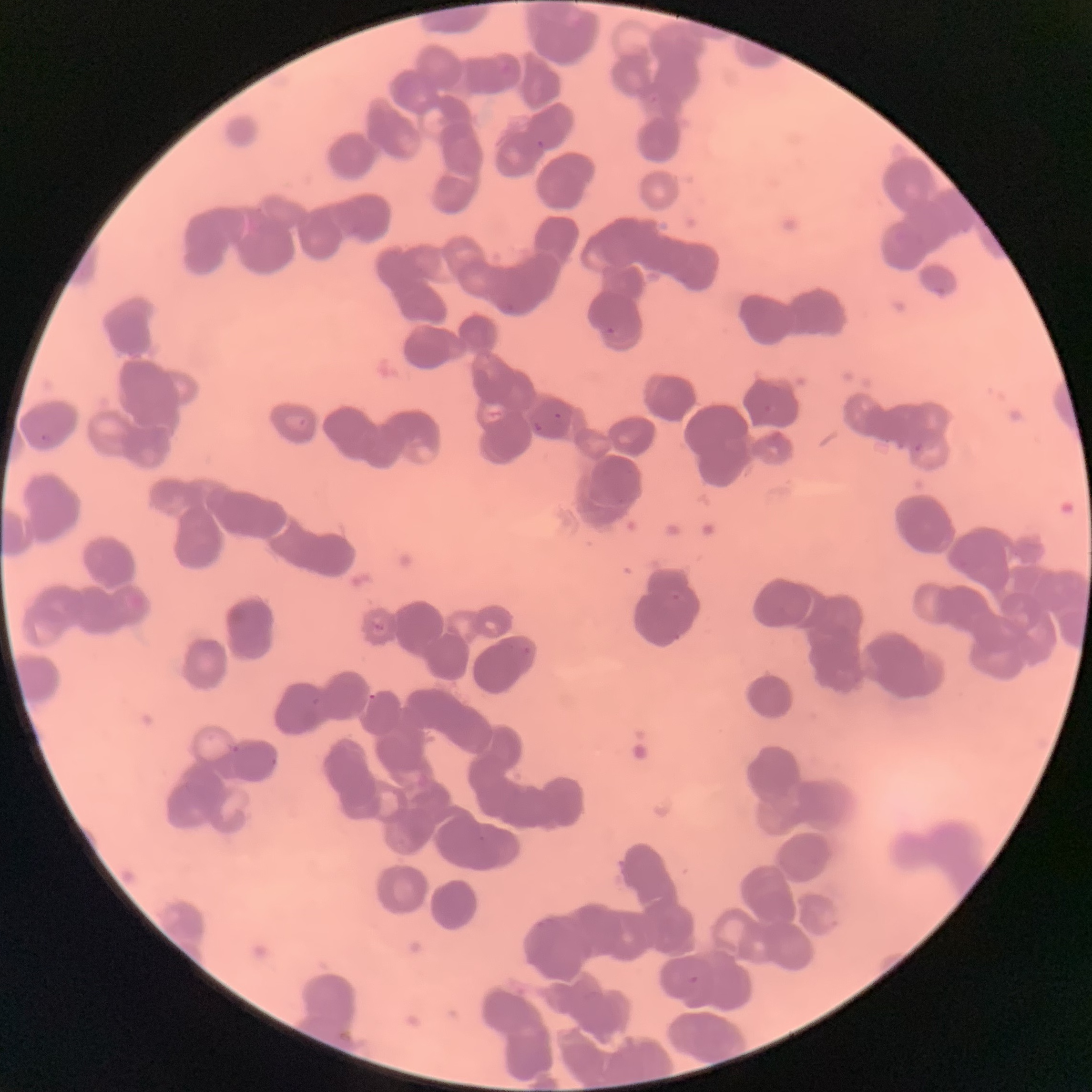 Approximate bounding boxes as [x1, y1, x2, y2] in pixels. Plasmodium parasite locations: [497, 59, 512, 74], [536, 139, 544, 150], [606, 327, 617, 335], [553, 411, 563, 421], [532, 420, 542, 433], [40, 432, 54, 443], [914, 440, 925, 452], [373, 621, 385, 632], [522, 645, 532, 656], [230, 744, 241, 755], [269, 755, 278, 767], [688, 974, 700, 986]. Image is 1092×1092 pixels. The red blood cells show rouleaux formation. Thin blood film. Optical microscopy.